State the blood parasite species.
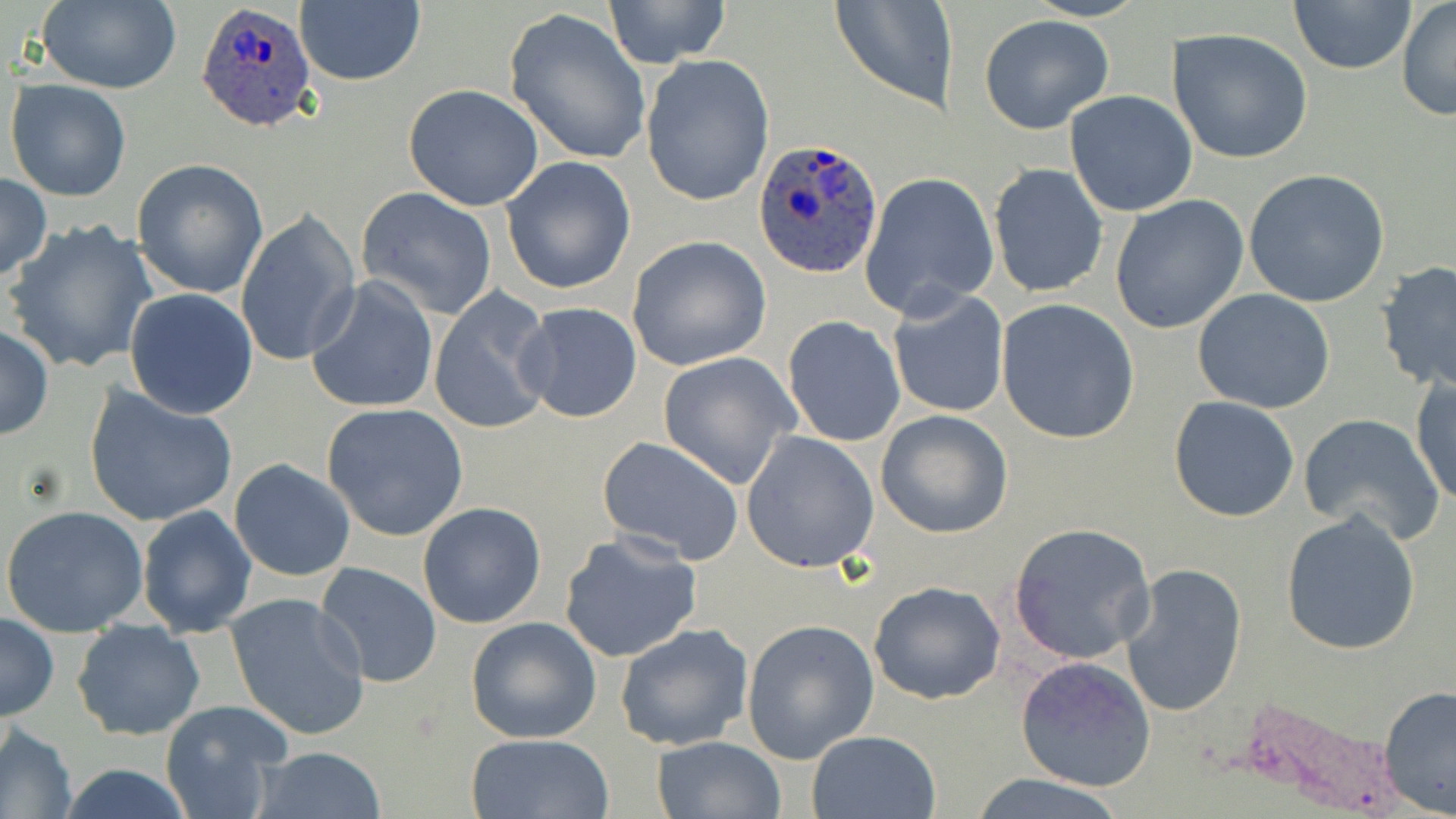
Plasmodium ovale.

Summary:
  - Coordinate format: approximate bounding boxes as named x1/y1/x2/y2 corners in pixels
  - Plasmodium ovale-infected red blood cell locations: (x1=195, y1=1, x2=322, y2=135), (x1=756, y1=136, x2=882, y2=280)
  - Uninfected red blood cell locations: (x1=295, y1=0, x2=424, y2=88), (x1=602, y1=0, x2=731, y2=68), (x1=830, y1=0, x2=955, y2=111), (x1=1287, y1=0, x2=1417, y2=76), (x1=1395, y1=0, x2=1456, y2=122), (x1=34, y1=2, x2=182, y2=93), (x1=503, y1=8, x2=652, y2=166), (x1=978, y1=14, x2=1114, y2=134), (x1=1167, y1=28, x2=1313, y2=164), (x1=641, y1=54, x2=774, y2=207), (x1=5, y1=78, x2=132, y2=201), (x1=403, y1=84, x2=548, y2=212), (x1=1064, y1=90, x2=1197, y2=216), (x1=499, y1=156, x2=636, y2=296), (x1=131, y1=158, x2=269, y2=300), (x1=989, y1=164, x2=1107, y2=298), (x1=1244, y1=169, x2=1391, y2=307), (x1=0, y1=171, x2=51, y2=282), (x1=861, y1=172, x2=998, y2=319), (x1=354, y1=186, x2=499, y2=322), (x1=1109, y1=194, x2=1249, y2=334), (x1=235, y1=210, x2=361, y2=367), (x1=4, y1=219, x2=158, y2=377), (x1=627, y1=237, x2=771, y2=371), (x1=1375, y1=260, x2=1456, y2=393), (x1=305, y1=276, x2=440, y2=414), (x1=124, y1=288, x2=258, y2=418), (x1=888, y1=288, x2=1010, y2=419), (x1=1192, y1=288, x2=1336, y2=414), (x1=427, y1=289, x2=557, y2=435), (x1=996, y1=299, x2=1139, y2=444), (x1=513, y1=302, x2=644, y2=424), (x1=782, y1=316, x2=906, y2=448), (x1=0, y1=325, x2=52, y2=441), (x1=657, y1=352, x2=801, y2=489), (x1=1410, y1=371, x2=1455, y2=507), (x1=83, y1=384, x2=239, y2=529), (x1=1167, y1=395, x2=1300, y2=522), (x1=322, y1=403, x2=469, y2=542), (x1=875, y1=410, x2=1014, y2=539), (x1=1298, y1=415, x2=1444, y2=545), (x1=740, y1=432, x2=881, y2=576), (x1=597, y1=436, x2=744, y2=565), (x1=228, y1=459, x2=356, y2=581), (x1=418, y1=502, x2=547, y2=629), (x1=2, y1=505, x2=149, y2=637), (x1=137, y1=506, x2=257, y2=638), (x1=1280, y1=511, x2=1423, y2=656), (x1=1008, y1=523, x2=1157, y2=666), (x1=558, y1=531, x2=703, y2=664), (x1=316, y1=562, x2=443, y2=688), (x1=1121, y1=562, x2=1247, y2=716), (x1=867, y1=580, x2=1007, y2=704), (x1=225, y1=593, x2=372, y2=742), (x1=0, y1=613, x2=58, y2=722), (x1=465, y1=616, x2=601, y2=744), (x1=741, y1=617, x2=880, y2=764), (x1=72, y1=619, x2=205, y2=739), (x1=614, y1=624, x2=754, y2=752), (x1=1016, y1=656, x2=1156, y2=792), (x1=1377, y1=684, x2=1456, y2=818), (x1=159, y1=701, x2=292, y2=818), (x1=1, y1=724, x2=77, y2=818), (x1=807, y1=729, x2=943, y2=819), (x1=461, y1=734, x2=617, y2=819), (x1=650, y1=735, x2=784, y2=819), (x1=252, y1=745, x2=386, y2=819), (x1=55, y1=763, x2=198, y2=819), (x1=963, y1=776, x2=1132, y2=819)
  - Field of view: one of a larger specimen
  - Image size: 1456×819 pixels
  - Stain: May-Grünwald-Giemsa
  - Preparation: thin blood film
  - Modality: light microscopy
  - Magnification: 1000x